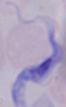

Summary:
  - Modality: micrograph
  - Magnification: 1000x
  - Identification: trypanosome